Assess for malaria.
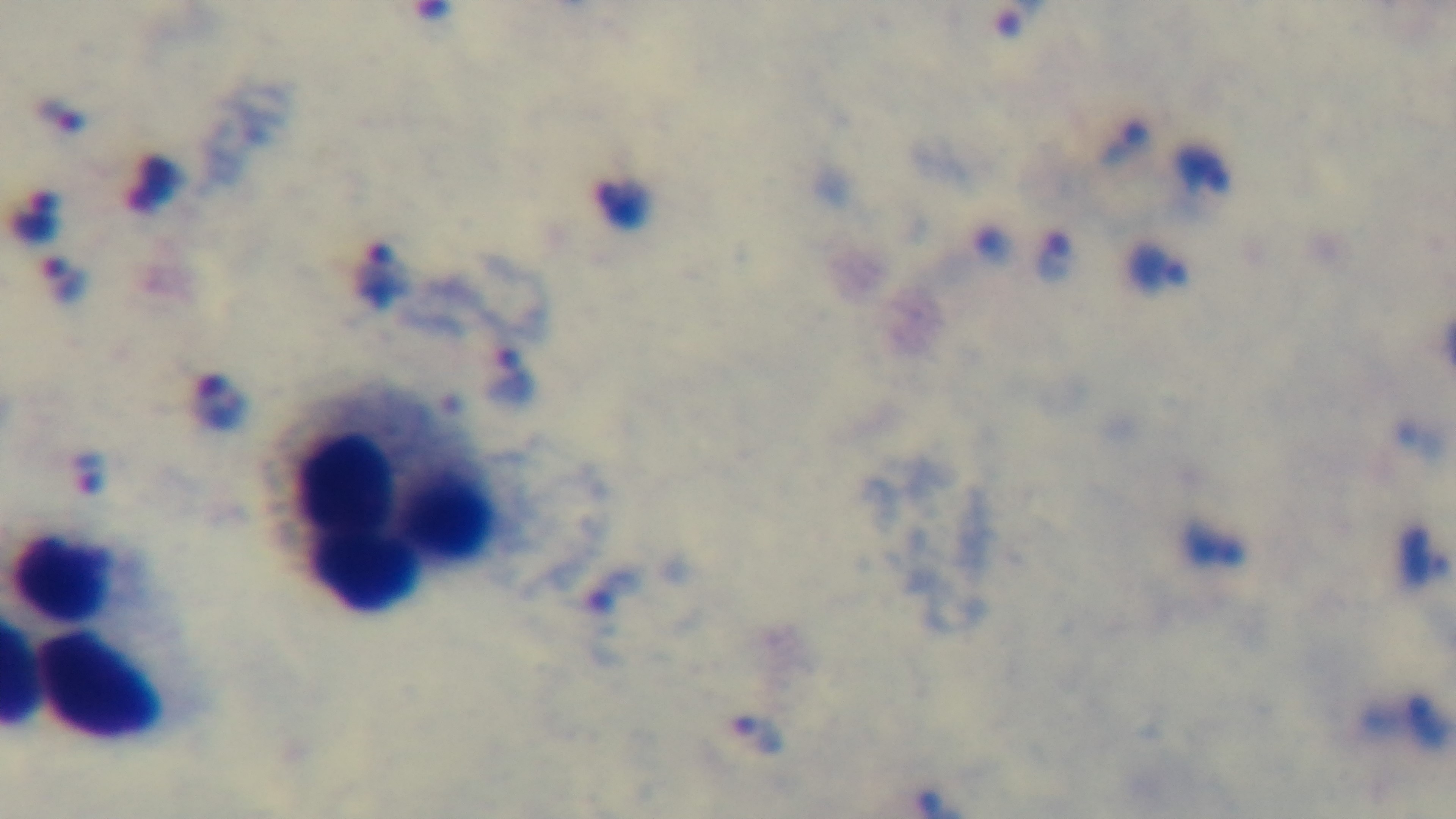

It is infected.

Giemsa-stained. Preparation: thick. Oil-immersion objective, 100x. Light microscopy. Mounted 4K digital camera. One field from the slide.